Classify this cell by malaria status.
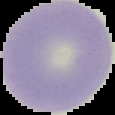

It is uninfected.

From a thin blood smear. Segmented cell region on a black background. Image is 115×115 pixels.